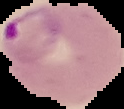
image_type: segmented cell region on a black background
preparation: thin blood smear
result: Plasmodium parasites identified
image_size: 124×109 pixels